Locate every Plasmodium vivax-infected red blood cell.
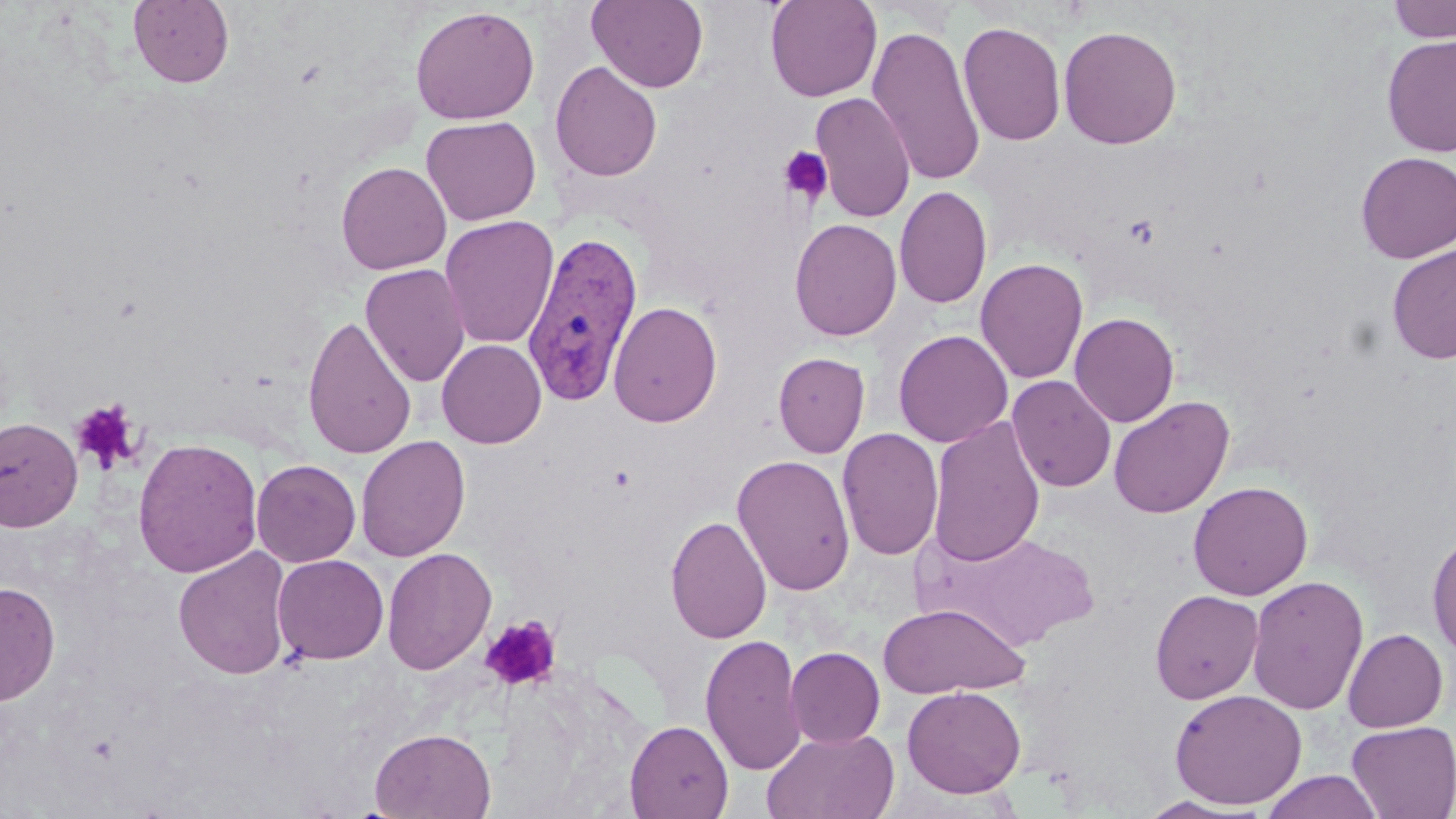

Approximate bounding boxes as (x1,y1)-(x2,y2) corner pairs in pixels.
Plasmodium vivax-infected red blood cells: (521,231)-(643,407).

Platelet locations: (778,145)-(833,206), (71,400)-(142,475), (480,616)-(562,693). Uninfected red blood cell locations: (587,0)-(709,92), (764,0)-(882,102), (1386,0)-(1456,43), (128,1)-(234,88), (410,6)-(539,125), (957,21)-(1066,146), (867,25)-(986,187), (1059,25)-(1182,149), (1381,34)-(1456,157), (549,60)-(663,182), (810,92)-(915,223), (421,115)-(541,225), (1355,152)-(1456,263), (336,161)-(451,274), (894,185)-(992,310), (439,215)-(559,350), (789,218)-(902,341), (1386,244)-(1456,364), (975,258)-(1088,384), (360,264)-(470,388), (608,300)-(723,428), (1070,312)-(1180,427), (302,314)-(417,460), (893,329)-(1013,448), (436,338)-(546,449), (773,352)-(870,458), (1006,374)-(1116,492), (1006,382)-(1235,499), (1108,395)-(1235,518), (0,416)-(83,531), (927,416)-(1046,568), (837,428)-(944,562), (356,435)-(470,561), (132,437)-(263,578), (732,453)-(856,596), (251,459)-(360,567), (1188,481)-(1313,600), (665,514)-(772,644), (1427,529)-(1456,660), (924,530)-(1099,650), (172,547)-(293,680), (382,547)-(497,676), (272,554)-(389,664), (1247,575)-(1368,715), (0,581)-(60,706), (1150,589)-(1263,704), (878,602)-(1030,698), (1342,628)-(1448,732), (700,632)-(807,775), (785,647)-(885,748), (902,685)-(1026,798), (1169,688)-(1307,810), (625,719)-(733,818), (1347,720)-(1456,818), (370,727)-(496,818), (761,727)-(900,819), (1261,770)-(1385,819), (1138,796)-(1260,818). Slide-level diagnosis: Plasmodium vivax. May-Grünwald-Giemsa stain. Thin blood film. 1000x magnification. Single field of view. Light microscopy. Image is 1456×819 pixels.